Give the extent of all Plasmodium falciparum-infected red blood cells.
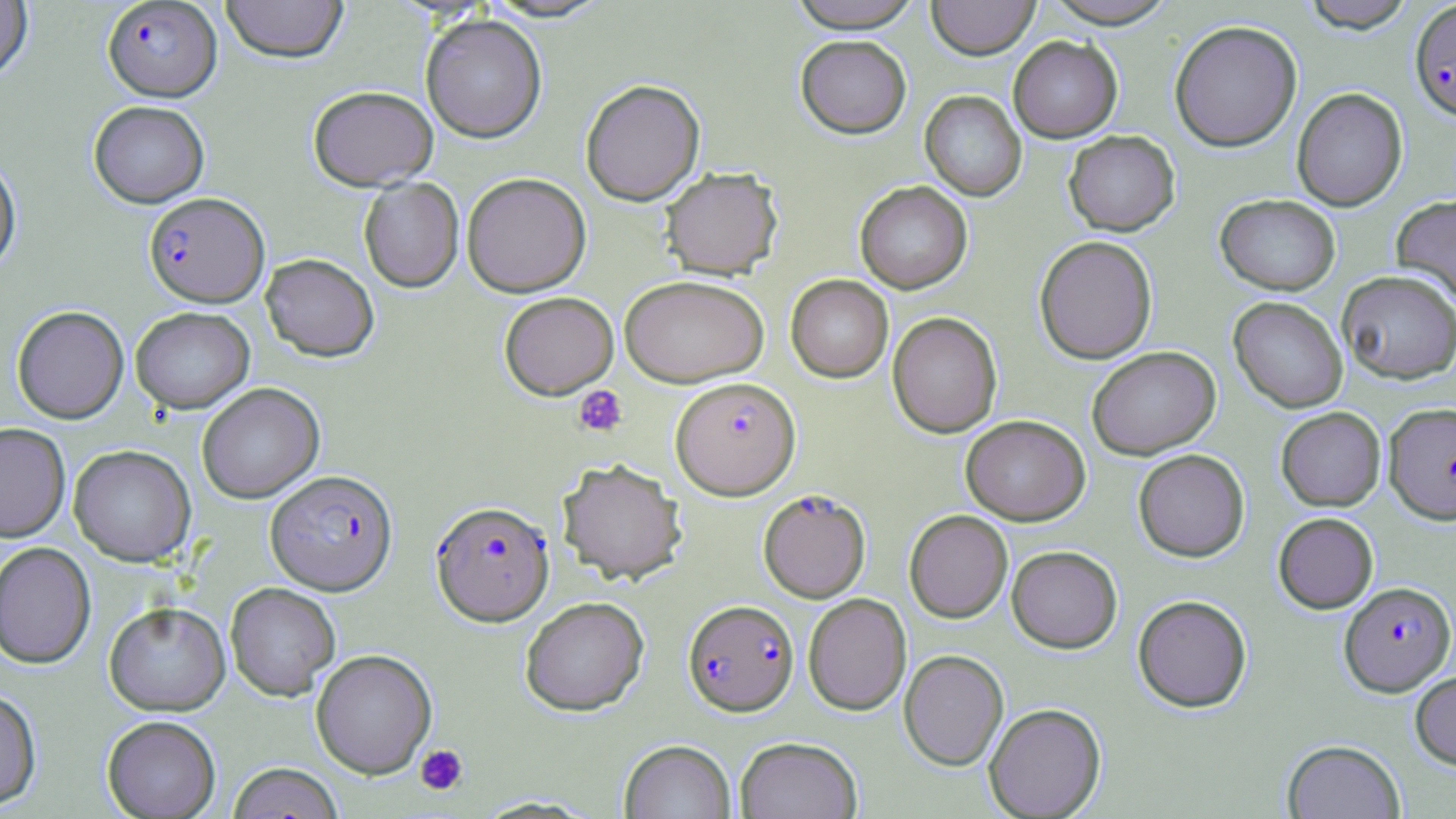
Approximate bounding boxes as named x1/y1/x2/y2 corners in pixels.
Plasmodium falciparum-infected red blood cells: (x1=102, y1=0, x2=222, y2=101), (x1=1410, y1=1, x2=1456, y2=121), (x1=143, y1=191, x2=269, y2=307), (x1=671, y1=376, x2=800, y2=499), (x1=1384, y1=402, x2=1456, y2=524), (x1=265, y1=469, x2=398, y2=595), (x1=758, y1=488, x2=871, y2=602), (x1=432, y1=500, x2=553, y2=625), (x1=1339, y1=581, x2=1455, y2=695), (x1=683, y1=599, x2=799, y2=716).

Platelet locations: (x1=573, y1=385, x2=628, y2=437), (x1=415, y1=744, x2=468, y2=795). Uninfected red blood cell locations: (x1=220, y1=0, x2=348, y2=62), (x1=481, y1=0, x2=614, y2=23), (x1=787, y1=0, x2=924, y2=32), (x1=927, y1=0, x2=1039, y2=59), (x1=1040, y1=0, x2=1180, y2=28), (x1=1300, y1=0, x2=1418, y2=32), (x1=0, y1=1, x2=33, y2=83), (x1=420, y1=14, x2=547, y2=143), (x1=1169, y1=20, x2=1302, y2=152), (x1=795, y1=35, x2=912, y2=138), (x1=1008, y1=36, x2=1122, y2=142), (x1=580, y1=78, x2=705, y2=206), (x1=307, y1=85, x2=438, y2=190), (x1=1291, y1=87, x2=1407, y2=211), (x1=920, y1=91, x2=1026, y2=201), (x1=88, y1=100, x2=209, y2=208), (x1=1063, y1=130, x2=1180, y2=236), (x1=0, y1=151, x2=21, y2=275), (x1=660, y1=166, x2=783, y2=280), (x1=461, y1=172, x2=591, y2=297), (x1=359, y1=177, x2=464, y2=293), (x1=855, y1=181, x2=973, y2=293), (x1=1215, y1=194, x2=1341, y2=295), (x1=1390, y1=194, x2=1456, y2=308), (x1=1034, y1=235, x2=1157, y2=364), (x1=260, y1=253, x2=379, y2=361), (x1=1337, y1=270, x2=1456, y2=384), (x1=619, y1=274, x2=769, y2=387), (x1=785, y1=274, x2=893, y2=383), (x1=499, y1=292, x2=618, y2=399), (x1=1228, y1=297, x2=1348, y2=413), (x1=11, y1=305, x2=129, y2=423), (x1=130, y1=306, x2=255, y2=413), (x1=887, y1=312, x2=1002, y2=438), (x1=1087, y1=346, x2=1221, y2=459), (x1=196, y1=383, x2=324, y2=503), (x1=1276, y1=407, x2=1386, y2=511), (x1=960, y1=414, x2=1090, y2=525), (x1=0, y1=422, x2=71, y2=543), (x1=68, y1=444, x2=196, y2=566), (x1=1133, y1=449, x2=1249, y2=561), (x1=557, y1=458, x2=687, y2=585), (x1=904, y1=510, x2=1012, y2=623), (x1=1273, y1=512, x2=1378, y2=613), (x1=0, y1=541, x2=96, y2=668), (x1=1006, y1=545, x2=1122, y2=653), (x1=225, y1=582, x2=341, y2=699), (x1=803, y1=593, x2=911, y2=715), (x1=1133, y1=594, x2=1252, y2=712), (x1=519, y1=596, x2=649, y2=715), (x1=104, y1=601, x2=230, y2=715), (x1=311, y1=649, x2=437, y2=778), (x1=899, y1=649, x2=1008, y2=769), (x1=1410, y1=670, x2=1456, y2=770), (x1=0, y1=688, x2=41, y2=810), (x1=984, y1=702, x2=1106, y2=818), (x1=101, y1=715, x2=221, y2=818), (x1=735, y1=736, x2=862, y2=819), (x1=619, y1=739, x2=736, y2=819), (x1=1282, y1=739, x2=1405, y2=818), (x1=226, y1=762, x2=345, y2=818). Slide-level diagnosis: Plasmodium falciparum. Thin blood smear. 1000x magnification. One field of a larger specimen. Optical microscopy. May-Grünwald-Giemsa stain. Image is 1456×819 pixels.